Give the position of every Plasmodium parasite visible.
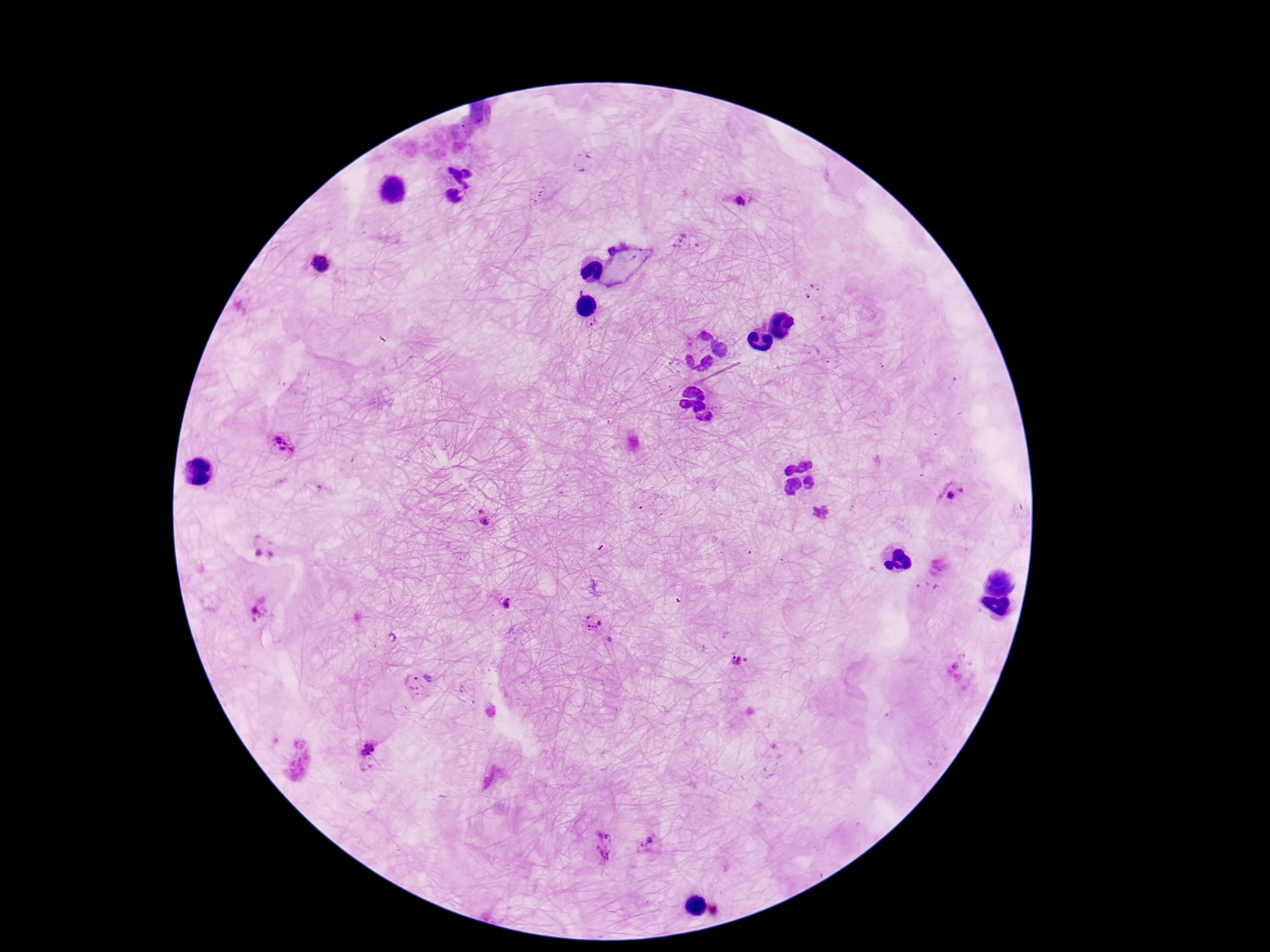
Approximate object centers, in pixels from the top-left corner.
Plasmodium parasites: (x=584, y=162), (x=742, y=198), (x=618, y=251), (x=323, y=264), (x=278, y=446), (x=952, y=494), (x=819, y=513), (x=485, y=517), (x=506, y=603), (x=258, y=610), (x=594, y=623), (x=740, y=659), (x=420, y=683), (x=367, y=753), (x=604, y=845), (x=646, y=845).

magnification: 100x
stain: Giemsa
field_of_view: one from this slide
preparation: thick blood film
patient_malaria_status: infected
capture: smartphone camera through the microscope eyepiece
image_size: 1270×952 pixels